Name the blood parasite species.
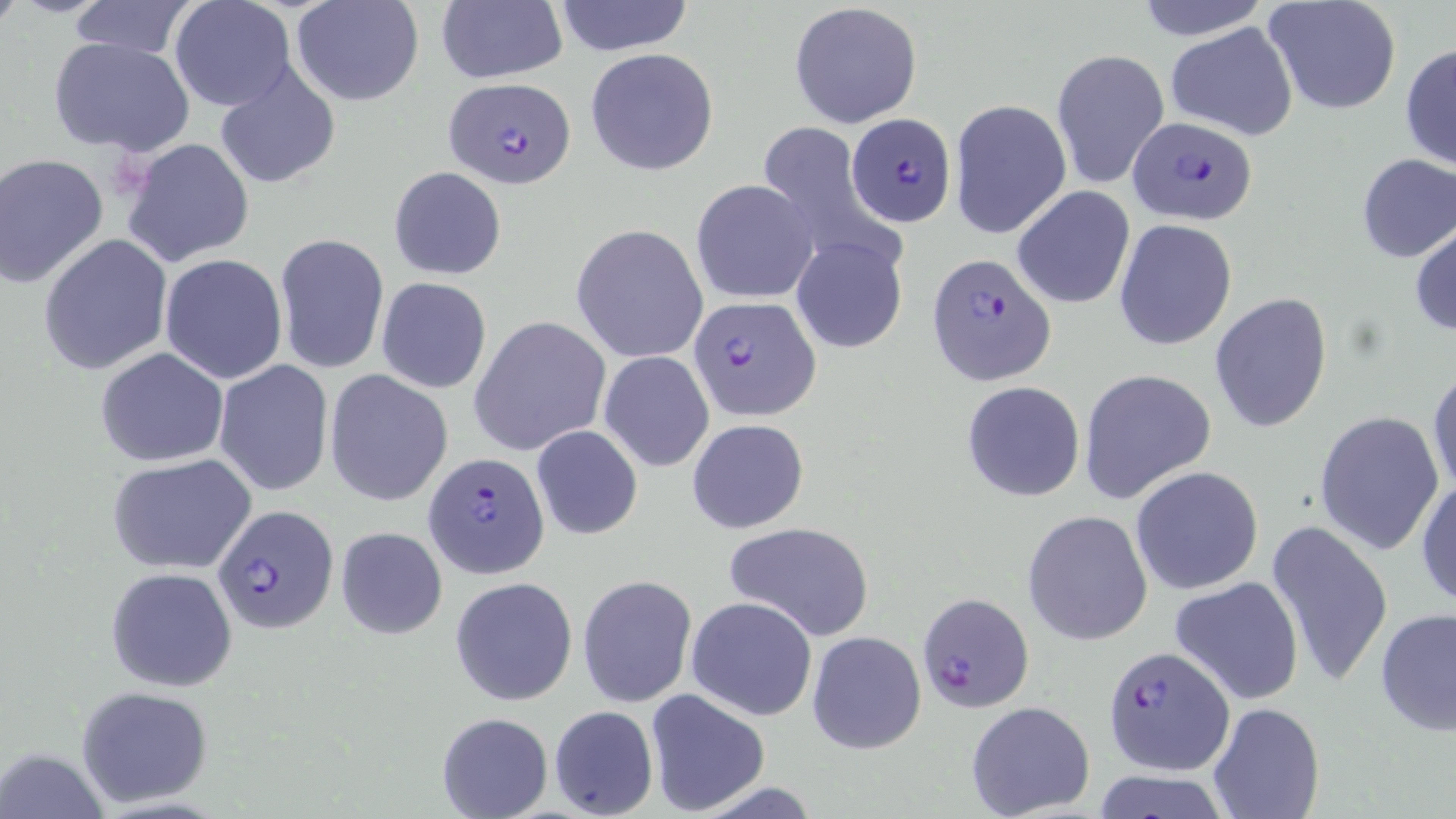
Plasmodium falciparum.

Approximate bounding boxes as [x1, y1, x2, y2] in pixels. Plasmodium falciparum-infected red blood cell locations: [443, 76, 575, 188], [846, 113, 956, 226], [1128, 115, 1258, 228], [927, 251, 1057, 387], [687, 295, 819, 422], [424, 452, 552, 578], [212, 505, 337, 632], [917, 591, 1034, 712], [1102, 643, 1234, 776]. Uninfected red blood cell locations: [66, 0, 199, 61], [170, 0, 295, 112], [292, 0, 423, 105], [436, 0, 566, 84], [553, 0, 695, 55], [1133, 0, 1272, 38], [1263, 0, 1403, 118], [790, 3, 923, 128], [1165, 23, 1299, 140], [48, 35, 193, 157], [1400, 43, 1456, 172], [585, 48, 720, 178], [1051, 48, 1170, 190], [214, 64, 341, 190], [948, 99, 1071, 237], [753, 122, 895, 263], [120, 137, 255, 267], [1, 153, 111, 289], [1355, 154, 1456, 263], [389, 167, 506, 280], [691, 180, 818, 303], [1012, 186, 1135, 309], [1114, 219, 1237, 351], [1411, 220, 1456, 338], [573, 224, 709, 364], [275, 234, 390, 374], [37, 235, 173, 377], [792, 236, 910, 355], [159, 254, 288, 384], [376, 276, 492, 394], [1209, 293, 1332, 435], [469, 317, 610, 456], [95, 346, 229, 467], [599, 350, 715, 472], [214, 361, 333, 497], [1427, 368, 1456, 501], [1079, 369, 1217, 507], [325, 370, 453, 507], [961, 380, 1085, 502], [1312, 410, 1445, 557], [687, 418, 809, 534], [531, 425, 643, 540], [107, 454, 258, 574], [1131, 466, 1264, 596], [1415, 477, 1456, 610], [1023, 509, 1153, 647], [1266, 519, 1393, 688], [723, 522, 878, 642], [336, 525, 449, 640], [105, 566, 239, 691], [578, 575, 697, 708], [450, 576, 577, 704], [1170, 576, 1305, 706], [686, 596, 819, 720], [1375, 606, 1455, 740], [806, 631, 926, 754], [76, 686, 216, 808], [644, 690, 770, 816], [966, 701, 1096, 818], [1209, 701, 1325, 818], [549, 705, 658, 819], [437, 712, 553, 819], [3, 747, 112, 819], [1090, 768, 1231, 818]. Captured at 1000x magnification. Thin blood film. Single field of view. Image is 1456×819 pixels. Optical microscopy. May-Grünwald-Giemsa stain.